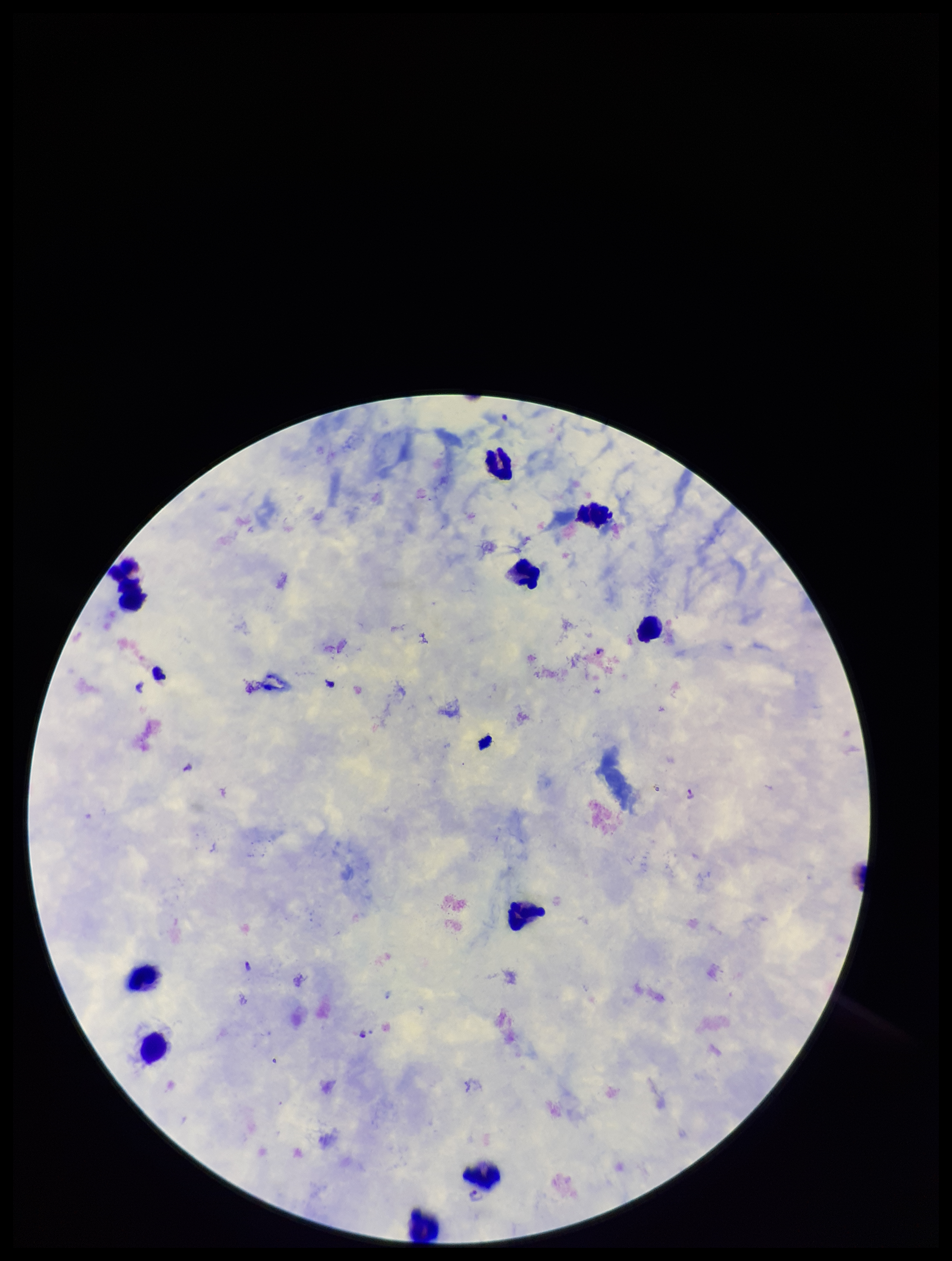
Parasite count: 3. Stained with Giemsa. Photographed through the microscope eyepiece with a smartphone camera. Preparation: thick. Patient malaria status: positive. Leukocyte count: 10. One field from this slide. Plasmodium parasites: detected. Species reported for this patient: Plasmodium falciparum. Image is 952×1261 pixels.